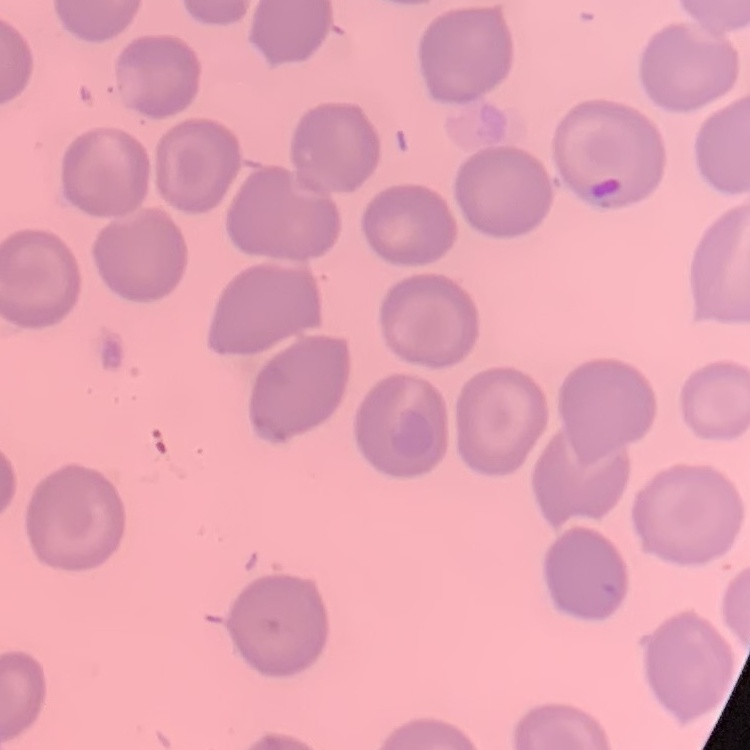
red blood cell morphology = no rouleaux formation
stain = Field's or Giemsa
preparation = thin blood smear
image type = one tile cut from a larger photomicrograph